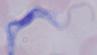

Captured at 1000x magnification. Micrograph. A trypanosome is shown.